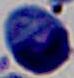
Summary:
  - Modality: micrograph
  - Identification: white blood cell
  - Magnification: 1000x